Draw a bounding box around every malaria parasite.
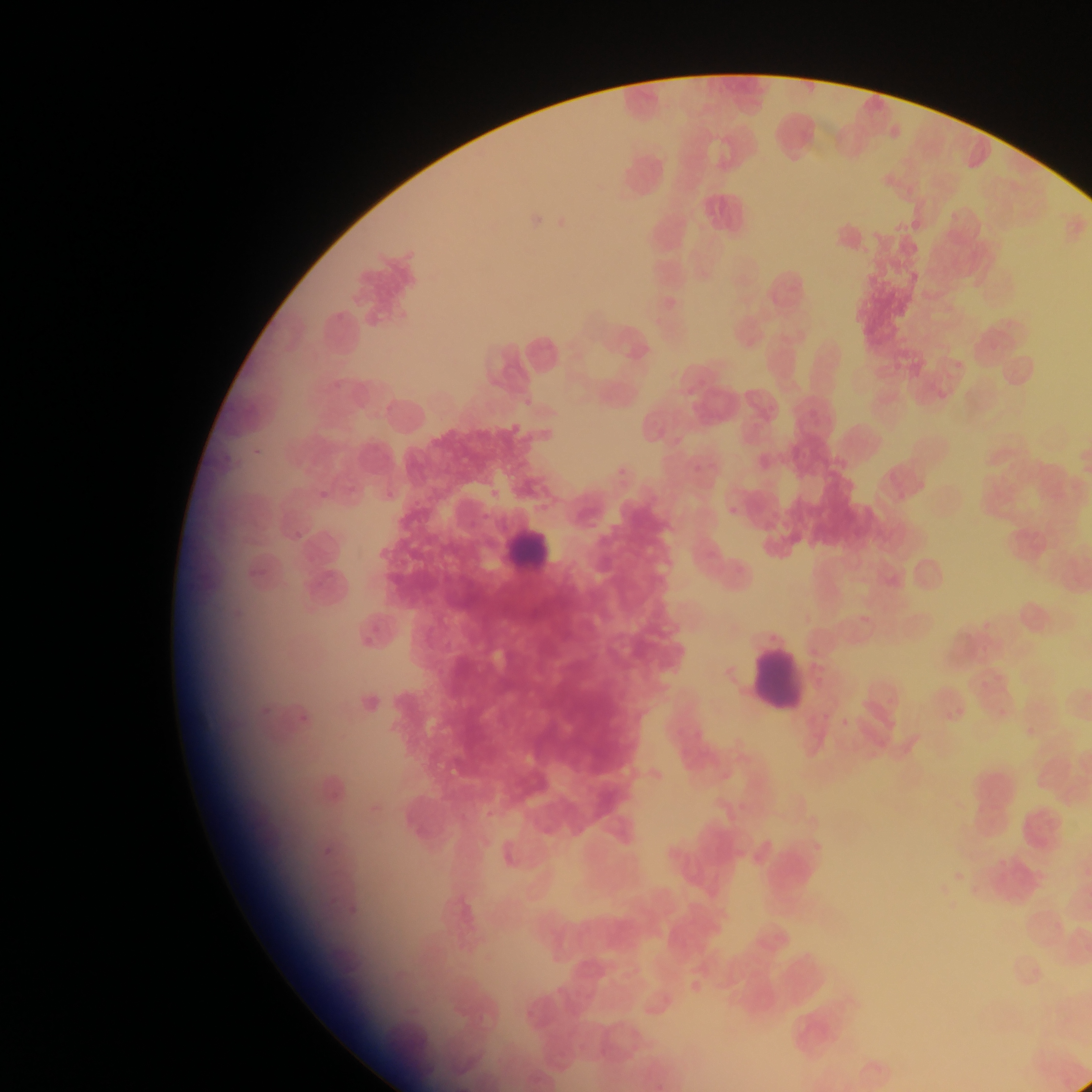

Approximate bounding boxes as {left, top, right, bottom} in pixels.
Malaria parasites: {519, 397, 535, 407}, {509, 428, 518, 438}, {250, 447, 262, 457}, {614, 464, 624, 479}, {691, 466, 703, 471}, {388, 486, 395, 499}, {318, 487, 327, 499}, {406, 494, 426, 505}, {727, 506, 743, 517}, {291, 525, 306, 540}, {257, 685, 278, 718}, {298, 714, 304, 722}, {321, 846, 327, 859}, {346, 905, 355, 915}.

preparation: thin blood film
field_of_view: single
leukocyte_locations: 'approximate bounding boxes as {left, top, right, bottom} in pixels: {611, 141, 674, 205}, {499, 517, 563, 577}, {746, 640, 809, 715}'
capture: mobile-phone photograph through a microscope
country: Ghana
image_size: 1092×1092 pixels